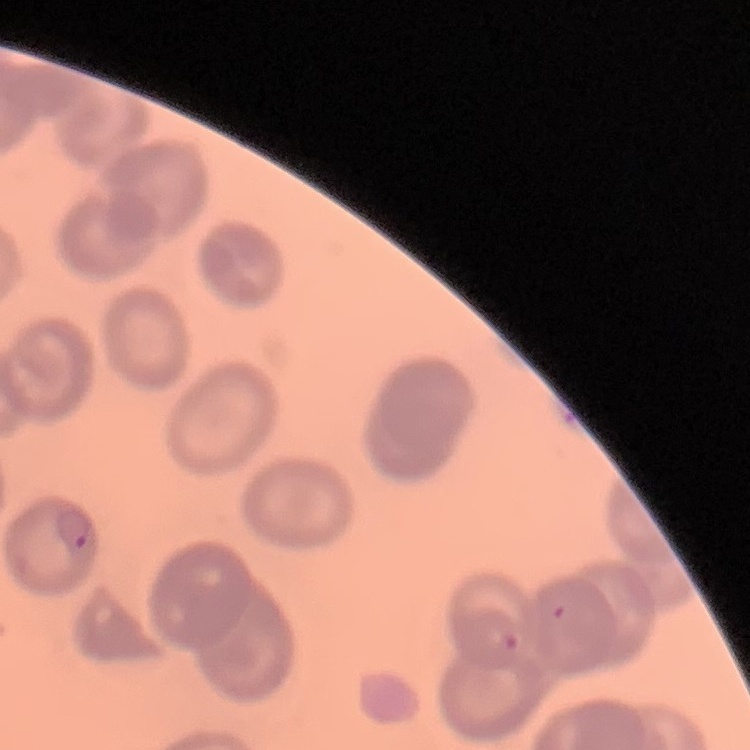

Summary:
  - Erythrocyte morphology: no rouleaux formation
  - Stain: Field's or Giemsa
  - Image type: square crop of a larger photomicrograph
  - Preparation: thin peripheral smear